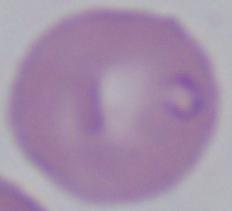
{
  "identification": "Babesia",
  "modality": "photomicrograph",
  "magnification": "1000x"
}